Report the malaria status.
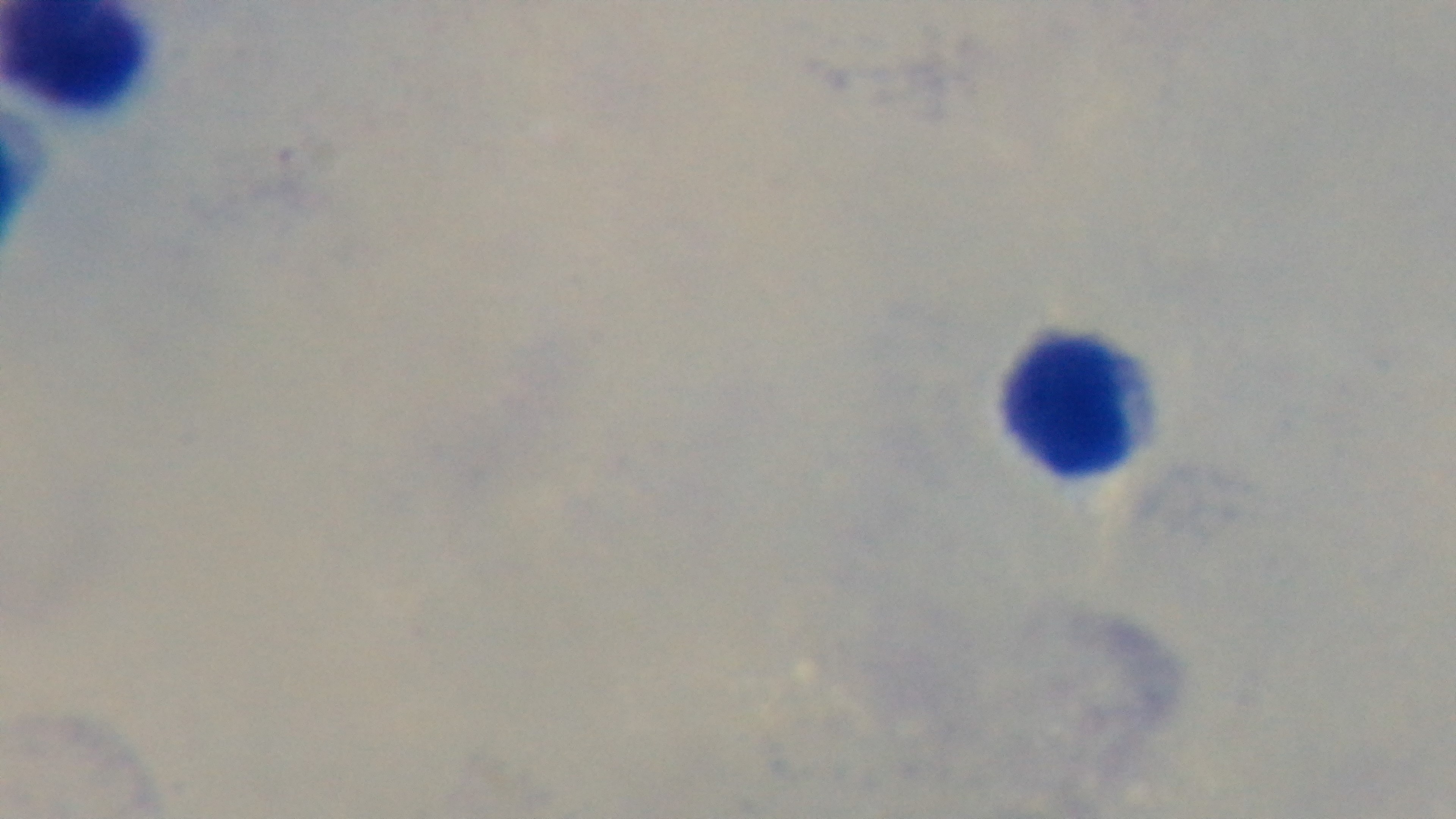
It is uninfected.

field of view = one from the slide
stain = Giemsa
preparation = thick blood film
objective = 100x oil immersion
capture = mounted 4K digital camera
modality = light microscopy